Locate and identify every blood parasite.
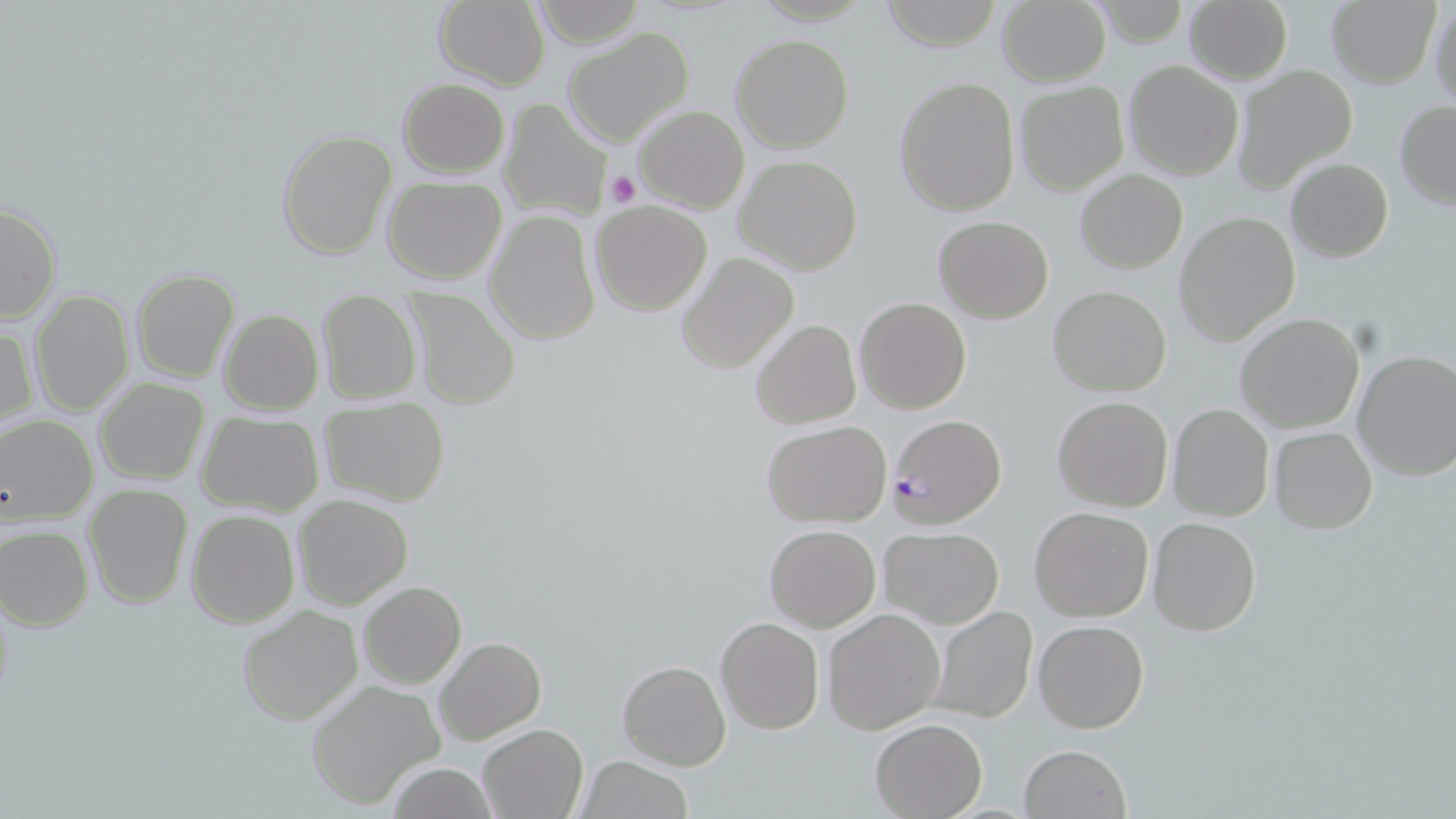
Approximate bounding boxes as (x1, y1, x2, y2) in pixels.
Plasmodium falciparum-infected red blood cells: (886, 414, 1009, 528).
No Plasmodium ovale, Plasmodium malariae, Plasmodium vivax, Babesia divergens, or Trypanosoma brucei observed.

Summary:
  - Uninfected red blood cell locations: (882, 0, 1001, 49), (995, 0, 1111, 87), (1184, 0, 1292, 84), (1327, 0, 1440, 87), (431, 1, 550, 89), (1428, 1, 1456, 111), (561, 26, 694, 147), (731, 34, 853, 153), (1124, 59, 1243, 180), (1232, 65, 1358, 194), (893, 75, 1021, 216), (396, 78, 509, 178), (1013, 80, 1129, 195), (498, 98, 615, 221), (1394, 100, 1456, 209), (634, 104, 749, 213), (276, 128, 399, 261), (733, 154, 863, 275), (1285, 158, 1392, 262), (1075, 168, 1188, 273), (383, 176, 507, 282), (589, 201, 713, 317), (0, 202, 60, 322), (483, 211, 601, 346), (1172, 211, 1301, 345), (932, 215, 1053, 324), (676, 252, 799, 373), (131, 268, 240, 384), (1048, 285, 1172, 397), (28, 289, 133, 415), (402, 290, 521, 412), (316, 292, 422, 405), (854, 296, 972, 414), (218, 309, 323, 415), (1234, 312, 1366, 434), (751, 319, 862, 430), (0, 322, 37, 433), (1352, 348, 1456, 483), (95, 379, 208, 485), (1052, 395, 1173, 512), (320, 399, 449, 505), (1166, 402, 1275, 522), (196, 412, 325, 518), (0, 415, 98, 524), (760, 419, 891, 527), (1269, 427, 1377, 533), (83, 483, 191, 608), (293, 493, 413, 610), (1028, 506, 1154, 622), (186, 509, 300, 627), (1149, 517, 1261, 635), (0, 525, 93, 630), (764, 525, 881, 632), (878, 526, 1005, 629), (359, 581, 466, 689), (236, 604, 364, 726), (926, 604, 1039, 724), (822, 608, 946, 735), (715, 616, 824, 735), (1032, 620, 1148, 734), (434, 636, 546, 744), (617, 660, 731, 770), (304, 679, 446, 809), (870, 718, 988, 818), (478, 725, 587, 817), (1018, 744, 1131, 819), (577, 755, 693, 819), (387, 764, 499, 818)
  - Platelet locations: (604, 169, 640, 208)
  - Slide-level diagnosis: Plasmodium falciparum
  - Preparation: thin blood film
  - Image size: 1456×819 pixels
  - Modality: optical microscopy
  - Field of view: one of a larger specimen
  - Stain: May-Grünwald-Giemsa
  - Magnification: 1000x